Locate every uninfected red blood cell.
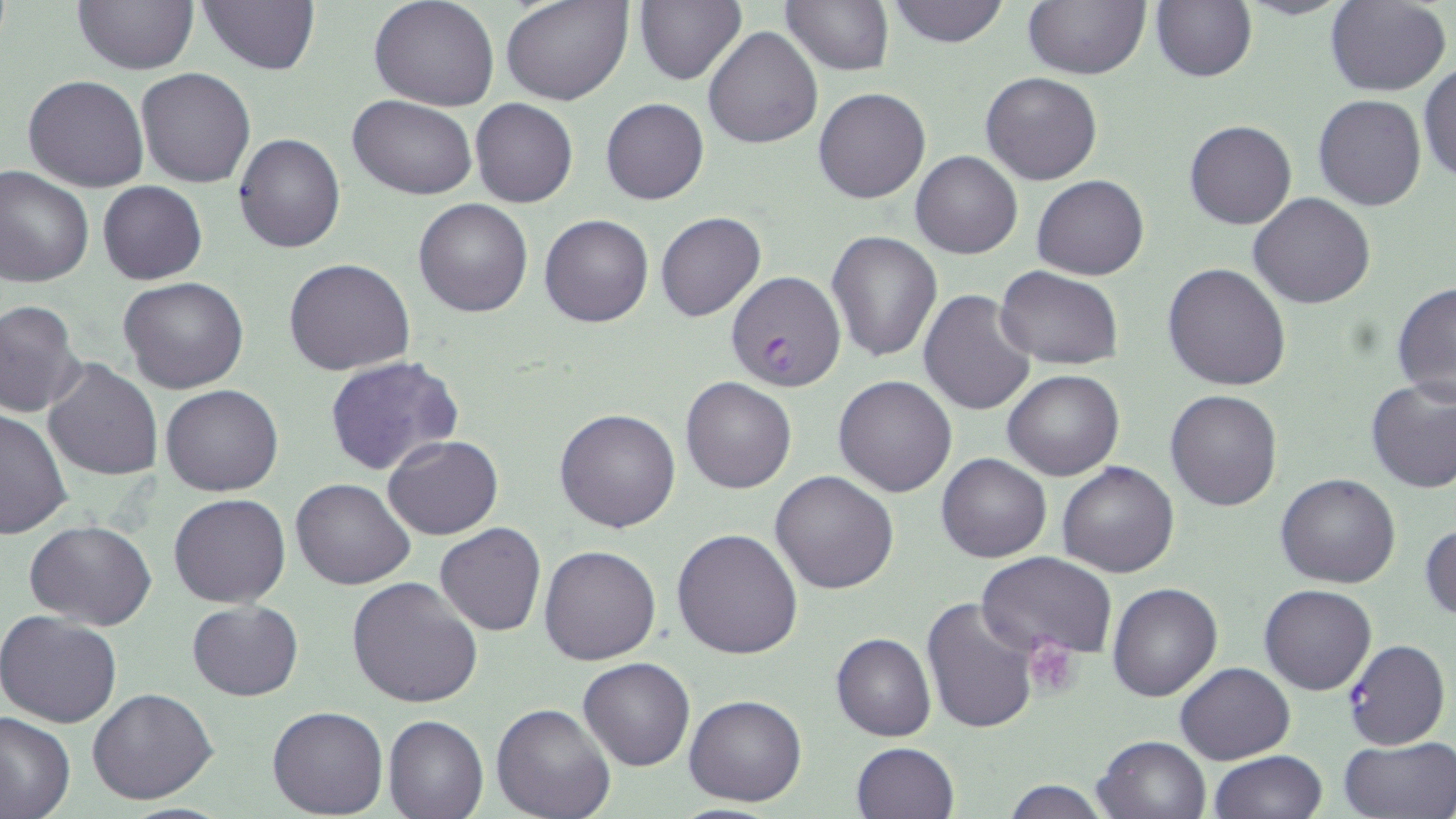
Approximate bounding boxes as (x1,y1)-(x2,y2) corner pairs in pixels.
Uninfected red blood cells: (197,0)-(322,75), (368,0)-(500,111), (503,0)-(633,105), (634,0)-(746,86), (782,0)-(893,74), (885,0)-(1009,47), (1022,0)-(1148,79), (1151,0)-(1257,83), (73,1)-(197,75), (1326,1)-(1451,96), (703,26)-(822,148), (1418,65)-(1456,185), (136,67)-(255,187), (980,71)-(1104,185), (23,74)-(149,192), (813,87)-(930,204), (1312,95)-(1428,211), (348,96)-(474,199), (600,98)-(708,204), (469,99)-(578,207), (1183,120)-(1296,230), (233,133)-(345,253), (911,151)-(1022,259), (0,164)-(94,286), (1032,175)-(1150,279), (97,180)-(206,285), (1250,192)-(1375,308), (412,198)-(533,318), (655,212)-(766,322), (540,214)-(653,327), (827,231)-(941,362), (283,257)-(415,375), (1163,262)-(1293,391), (994,267)-(1124,370), (118,275)-(249,394), (1392,278)-(1456,410), (918,288)-(1037,414), (0,300)-(86,418), (325,355)-(465,477), (43,358)-(162,481), (1001,369)-(1124,480), (833,374)-(958,497), (680,376)-(796,493), (1364,377)-(1456,493), (160,385)-(285,496), (1164,389)-(1283,510), (0,407)-(74,541), (554,407)-(682,533), (382,434)-(503,540), (936,452)-(1051,563), (1057,460)-(1179,578), (769,471)-(898,594), (1275,473)-(1402,589), (291,477)-(416,589), (168,492)-(291,607), (26,520)-(156,631), (1420,520)-(1455,624), (434,522)-(546,636), (671,529)-(803,661), (538,545)-(662,665), (978,553)-(1118,659), (347,577)-(483,708), (1107,582)-(1221,702), (1259,584)-(1376,695), (921,596)-(1040,735), (188,601)-(303,700), (0,611)-(123,729), (831,633)-(935,741), (577,657)-(695,771), (1174,662)-(1295,764), (87,687)-(219,805), (683,694)-(807,807), (493,703)-(614,819), (267,705)-(388,817), (0,710)-(75,819), (383,715)-(487,818), (1093,735)-(1210,819), (1339,736)-(1456,818), (850,742)-(959,819), (1209,751)-(1329,819), (999,779)-(1116,818).

Summary:
  - Plasmodium falciparum-infected red blood cell locations: (725,271)-(846,393), (1340,640)-(1449,750)
  - Platelet locations: (1024,636)-(1081,700)
  - Slide-level diagnosis: Plasmodium falciparum
  - Preparation: thin blood smear
  - Stain: May-Grünwald-Giemsa
  - Modality: light microscopy
  - Field of view: one of a larger specimen
  - Magnification: 1000x
  - Image size: 1456×819 pixels